Classify this cell by malaria status.
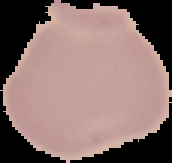
Uninfected.

Image is 172×163 pixels. From a thin blood smear. Segmented cell region on a black background.